Describe the morphology of the red blood cells.
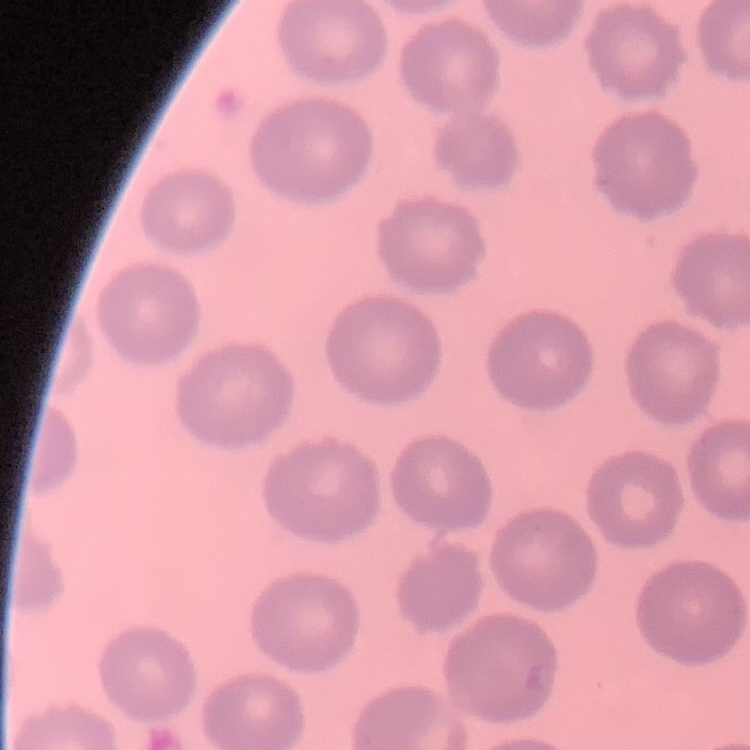

They show no rouleaux formation.

Stained with either Field's or Giemsa. One tile cut from a larger photomicrograph. Thin peripheral smear.